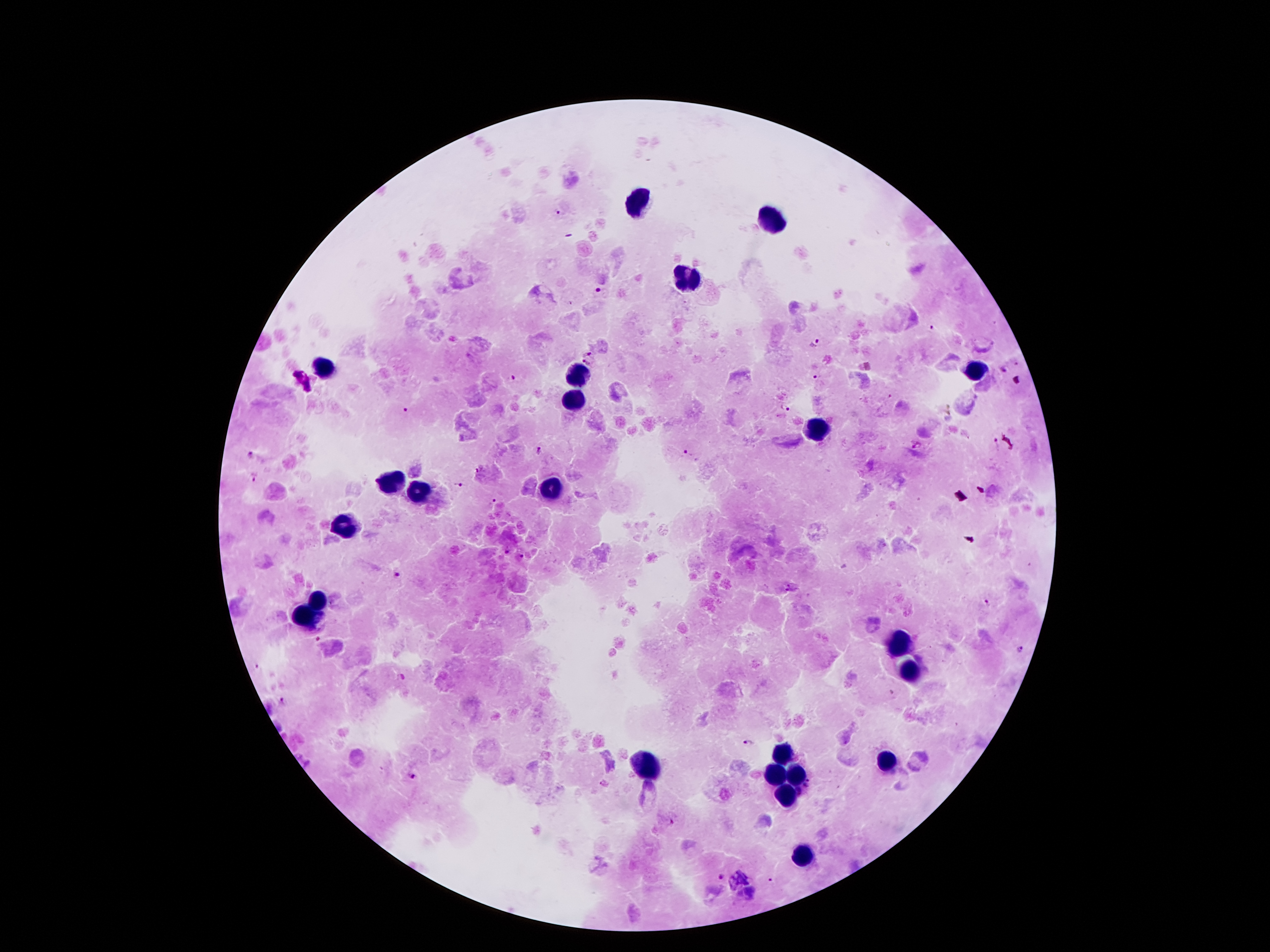

Approximate centers as [x, y] in pixels. Leukocyte locations: [637, 200], [776, 219], [685, 278], [324, 368], [578, 372], [975, 372], [572, 402], [815, 433], [389, 479], [551, 488], [416, 492], [347, 528], [318, 599], [307, 616], [899, 643], [910, 670], [784, 752], [885, 763], [647, 765], [773, 773], [797, 773], [786, 792], [803, 855]. Malaria parasite locations: [560, 210], [599, 290], [931, 327], [815, 341], [587, 353], [587, 363], [1002, 369], [819, 376], [514, 378], [787, 408], [407, 410], [996, 444], [916, 445], [538, 450], [688, 451], [252, 455], [480, 468], [254, 477], [458, 484], [492, 502], [506, 551], [524, 556], [398, 575], [792, 583], [787, 592], [982, 605], [319, 637], [1020, 648], [400, 677], [281, 701], [748, 744], [411, 775], [672, 821], [722, 878]. Photographed through the microscope eyepiece with a smartphone camera. 100x magnification. Giemsa stain. Patient malaria status: positive for Plasmodium falciparum. Thick peripheral-blood smear. Image is 1270×952 pixels. Single field of view.